Assess this cell for malaria.
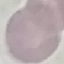
Uninfected.

Giemsa stain. Acquired by smartphone through the microscope eyepiece. Thin smear of blood. Automatically extracted cell patch, resized to 64 × 64 pixels.